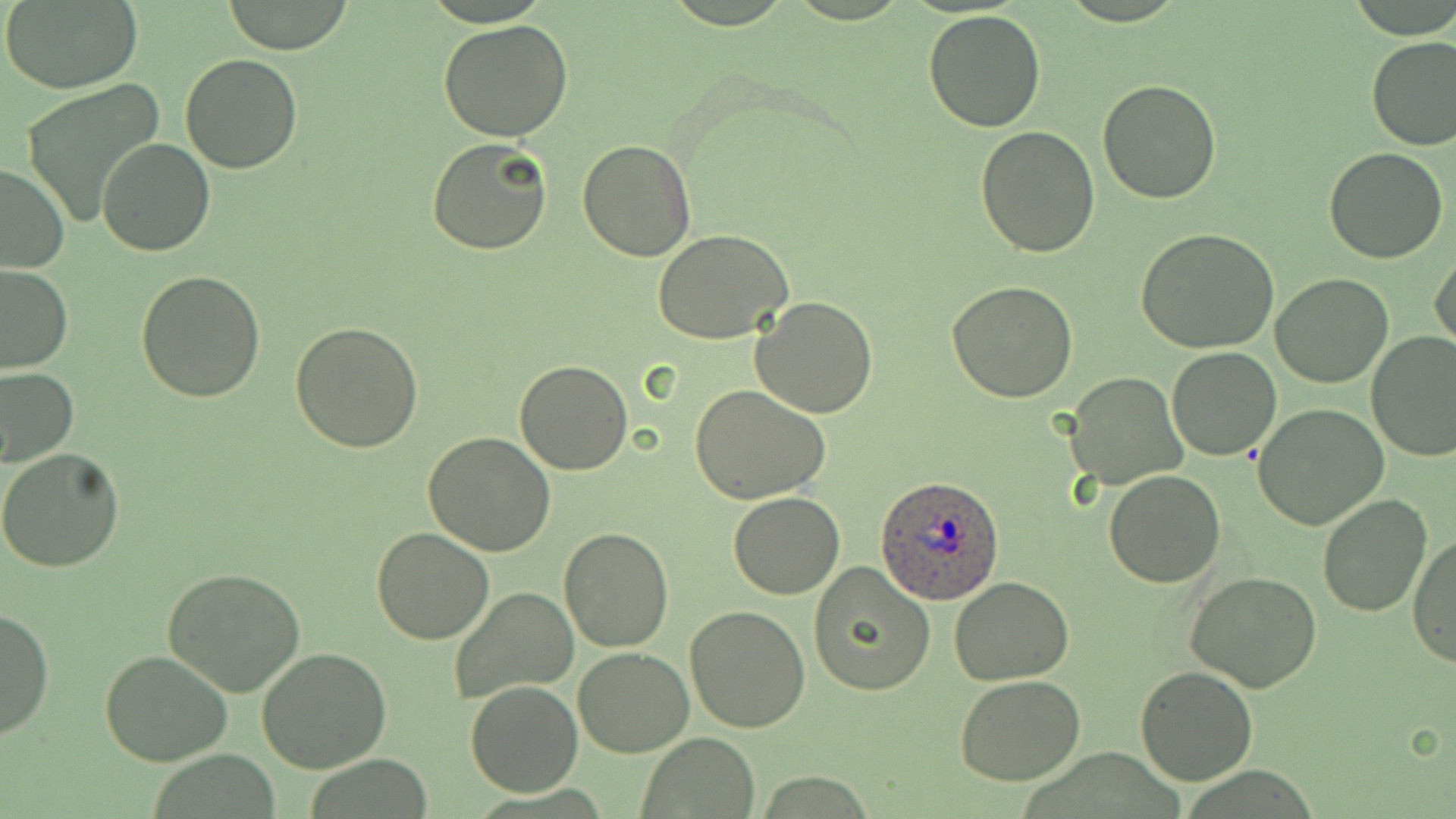
Summary:
  - Coordinate format: approximate bounding boxes as named x1/y1/x2/y2 corners in pixels
  - Plasmodium ovale-infected red blood cell locations: (x1=875, y1=476, x2=1004, y2=604)
  - Uninfected red blood cell locations: (x1=2, y1=1, x2=143, y2=92), (x1=220, y1=2, x2=355, y2=53), (x1=922, y1=9, x2=1047, y2=131), (x1=438, y1=19, x2=574, y2=140), (x1=1365, y1=34, x2=1455, y2=151), (x1=179, y1=53, x2=305, y2=173), (x1=19, y1=78, x2=166, y2=230), (x1=1097, y1=80, x2=1222, y2=204), (x1=975, y1=126, x2=1099, y2=257), (x1=427, y1=136, x2=552, y2=256), (x1=98, y1=139, x2=214, y2=256), (x1=577, y1=139, x2=699, y2=262), (x1=1324, y1=148, x2=1448, y2=263), (x1=0, y1=161, x2=68, y2=274), (x1=1136, y1=229, x2=1282, y2=353), (x1=654, y1=230, x2=794, y2=344), (x1=1432, y1=247, x2=1456, y2=355), (x1=0, y1=264, x2=73, y2=374), (x1=135, y1=270, x2=265, y2=403), (x1=1270, y1=273, x2=1395, y2=388), (x1=947, y1=282, x2=1078, y2=404), (x1=750, y1=297, x2=879, y2=418), (x1=290, y1=319, x2=424, y2=452), (x1=1366, y1=331, x2=1456, y2=461), (x1=1167, y1=347, x2=1282, y2=461), (x1=515, y1=359, x2=633, y2=475), (x1=0, y1=365, x2=78, y2=468), (x1=1066, y1=374, x2=1187, y2=492), (x1=689, y1=383, x2=832, y2=504), (x1=1253, y1=404, x2=1389, y2=532), (x1=423, y1=432, x2=555, y2=555), (x1=0, y1=448, x2=125, y2=573), (x1=1103, y1=470, x2=1225, y2=588), (x1=728, y1=493, x2=845, y2=599), (x1=1317, y1=493, x2=1432, y2=617), (x1=370, y1=526, x2=493, y2=644), (x1=558, y1=528, x2=675, y2=651), (x1=1410, y1=532, x2=1455, y2=670), (x1=807, y1=563, x2=935, y2=697), (x1=163, y1=567, x2=305, y2=697), (x1=1183, y1=571, x2=1323, y2=693), (x1=950, y1=577, x2=1074, y2=685), (x1=448, y1=587, x2=580, y2=705), (x1=685, y1=604, x2=813, y2=733), (x1=0, y1=606, x2=53, y2=741), (x1=574, y1=647, x2=693, y2=757), (x1=255, y1=648, x2=392, y2=774), (x1=101, y1=649, x2=233, y2=767), (x1=1134, y1=665, x2=1257, y2=785), (x1=954, y1=675, x2=1086, y2=785), (x1=465, y1=681, x2=582, y2=797), (x1=639, y1=734, x2=760, y2=818)
  - Slide-level diagnosis: Plasmodium ovale
  - Preparation: thin blood film
  - Field of view: one of a larger specimen
  - Image size: 1456×819 pixels
  - Magnification: 1000x
  - Modality: optical microscopy
  - Stain: May-Grünwald-Giemsa